Assess for malaria.
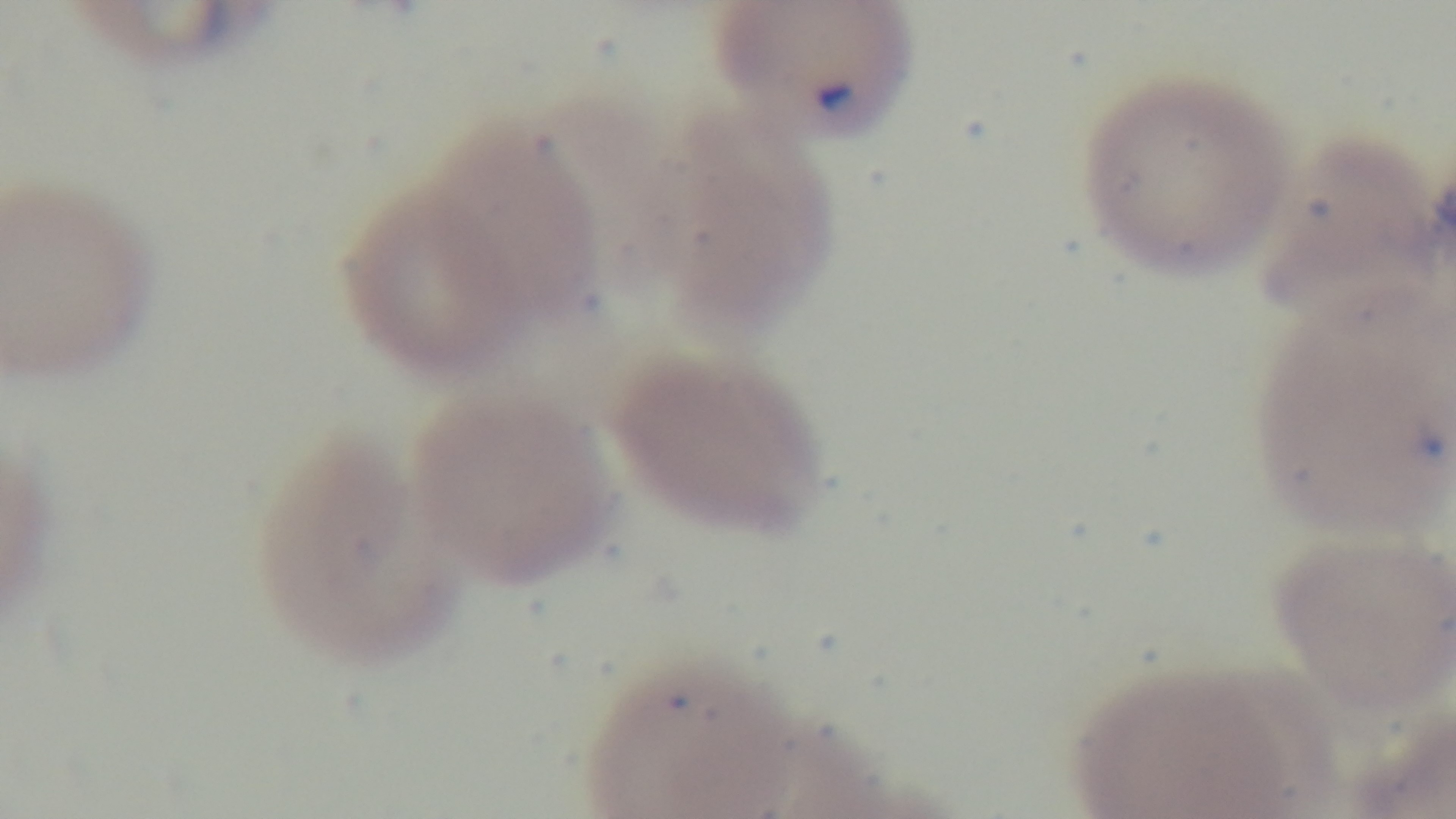
It is infected.

Preparation: thin blood film. Light microscopy. Mounted 4K digital camera. One field from the slide. Giemsa stain. Oil-immersion objective, 100x.